Locate every Plasmodium parasite.
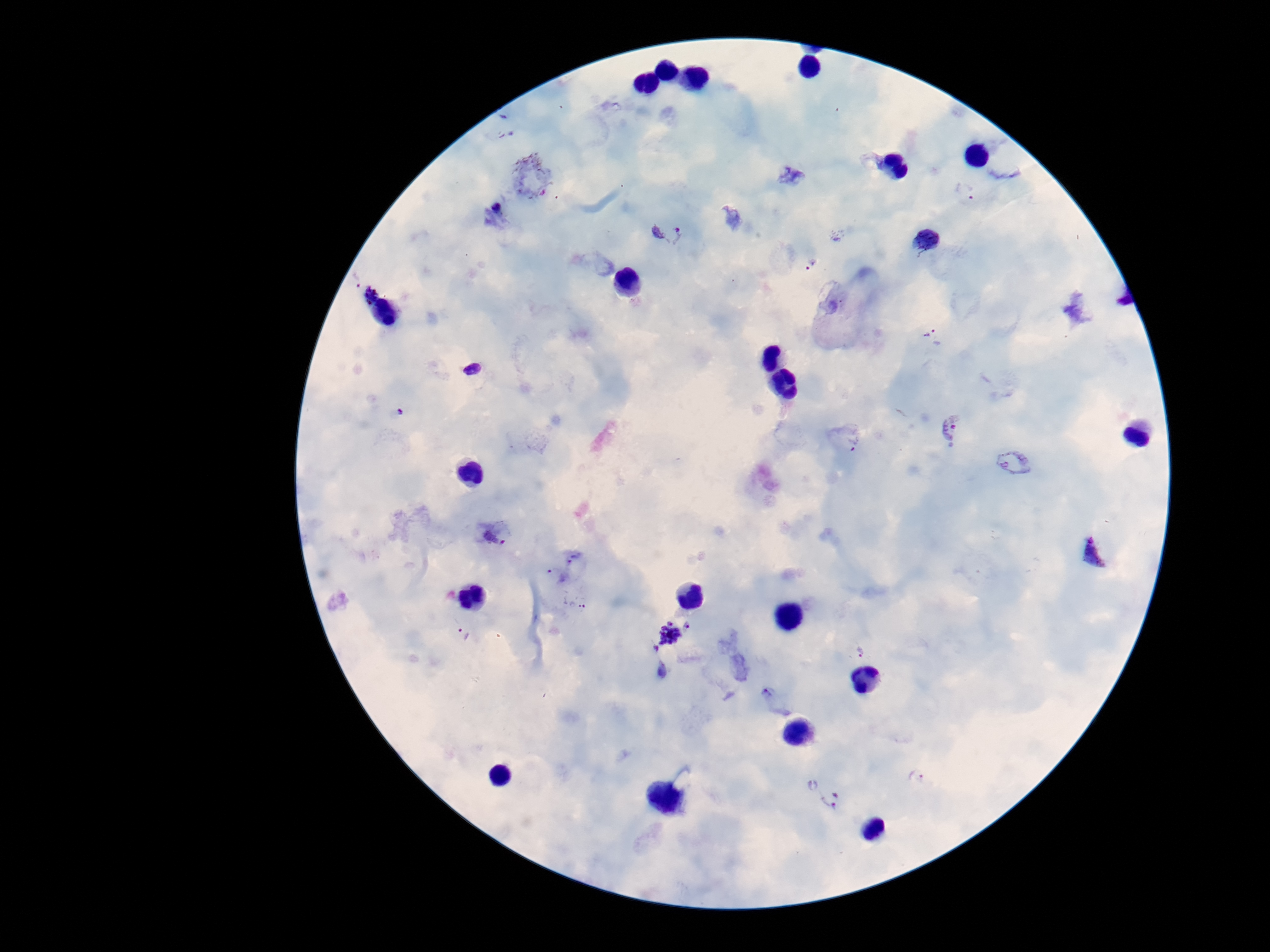
Approximate centers as {x, y} in pixels.
Plasmodium parasites: {870, 160}, {790, 176}, {531, 177}, {964, 192}, {666, 230}, {927, 241}, {809, 264}, {354, 276}, {370, 296}, {934, 338}, {473, 369}, {949, 428}, {850, 440}, {1014, 462}, {494, 537}, {1095, 552}, {575, 556}, {556, 575}, {575, 603}, {687, 626}, {667, 633}, {461, 634}, {655, 650}, {861, 652}, {661, 670}, {777, 700}, {919, 778}, {830, 799}.

image_size: 1270×952 pixels
field_of_view: single
stain: Giemsa
preparation: thick blood smear
capture: smartphone camera through the microscope eyepiece
magnification: 100x
patient_malaria_status: infected